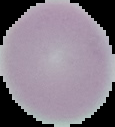
{
  "image_type": "cell region segmented out of the field of view; surrounding area masked to black",
  "result": "negative for malaria parasites",
  "preparation": "thin blood smear",
  "image_size": "115×127 pixels"
}